Assess the morphology of the red blood cells.
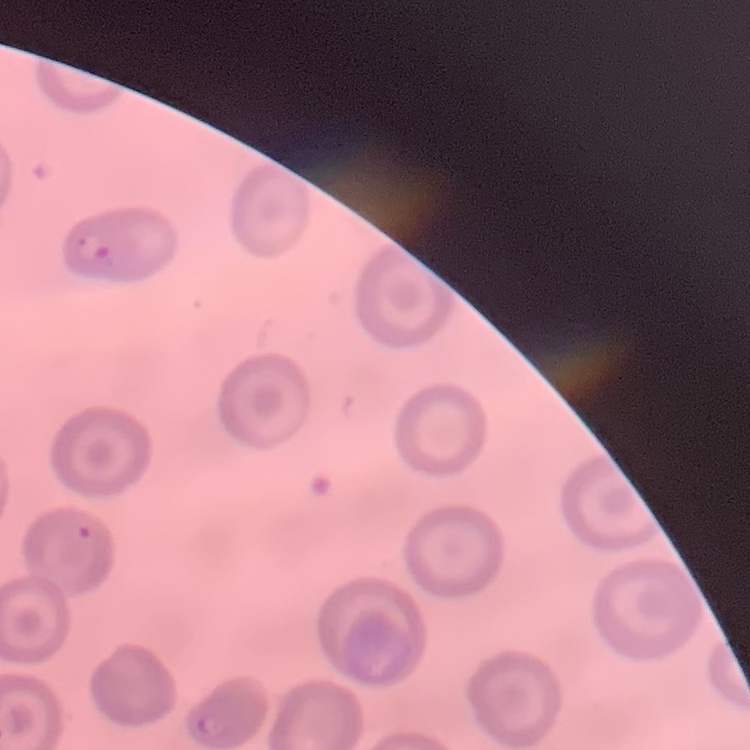
They show no rouleaux formation.

preparation = thin peripheral smear
stain = Field's or Giemsa
image type = square crop of a larger photomicrograph